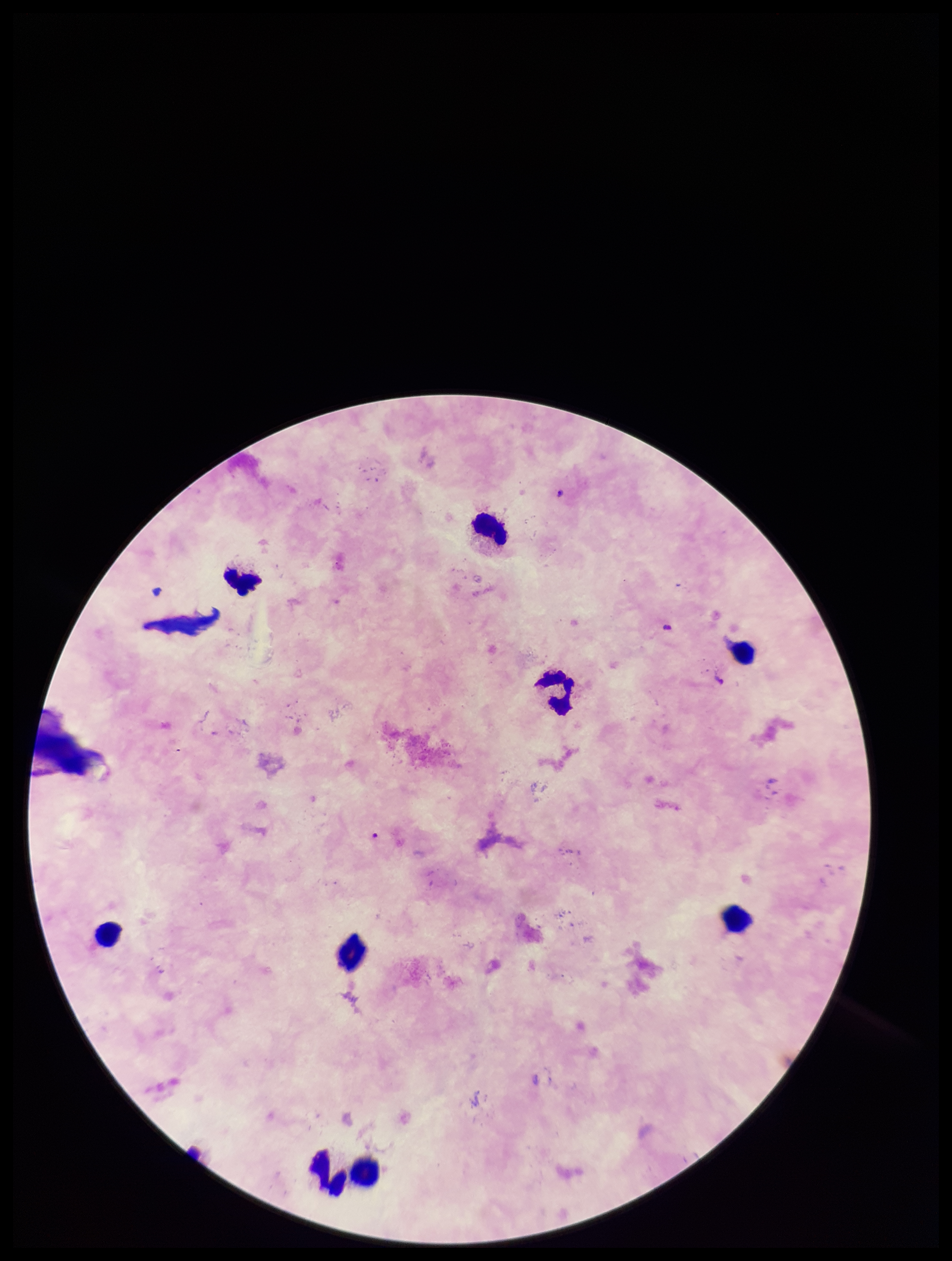
Giemsa stain. Parasite count: 1. Preparation: thick blood smear. Patient malaria status: infected. Image is 952×1261 pixels. Leukocyte count: 9. Plasmodium parasites: detected. Smartphone photograph taken through the eyepiece of a microscope. Species reported for this patient: Plasmodium falciparum. One field from this slide.